Locate every Plasmodium malariae-infected red blood cell.
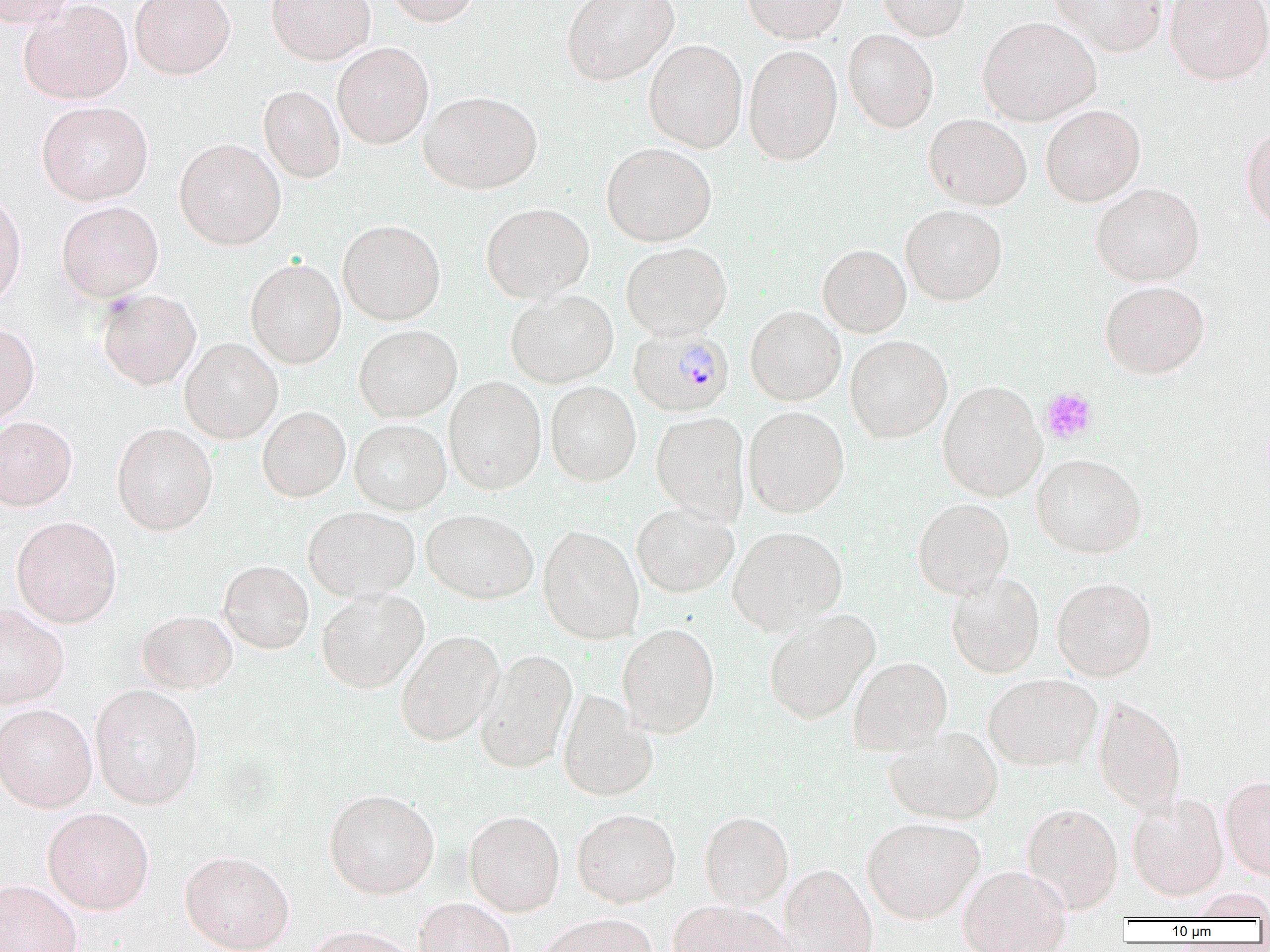
Approximate bounding boxes as (x1,y1)-(x2,y2) corner pairs in pixels.
Plasmodium malariae-infected red blood cells: (629,326)-(735,416).

{
  "slide_level_diagnosis": "Plasmodium malariae",
  "preparation": "thin blood film",
  "modality": "light microscopy",
  "uninfected_red_blood_cell_locations": "approximate bounding boxes as (x1,y1)-(x2,y2) corner pairs in pixels: (0,0)-(77,28), (130,0)-(235,79), (266,0)-(375,65), (384,0)-(481,27), (561,0)-(679,85), (742,0)-(848,43), (878,0)-(970,41), (1050,0)-(1167,56), (1165,0)-(1270,84), (19,1)-(133,105), (978,16)-(1101,125), (843,29)-(938,133), (643,39)-(748,152), (332,42)-(434,149), (743,45)-(843,165), (259,85)-(346,183), (419,90)-(543,194), (36,101)-(152,205), (1040,105)-(1145,206), (917,113)-(1018,301), (924,113)-(1032,210), (1240,124)-(1270,231), (174,138)-(286,249), (601,142)-(717,246), (1091,183)-(1204,286), (0,191)-(27,310), (56,201)-(164,301), (481,202)-(594,302), (901,204)-(1007,306), (338,219)-(445,325), (621,241)-(732,339), (817,243)-(911,337), (245,258)-(346,368), (1100,280)-(1209,378), (96,288)-(202,390), (505,289)-(618,387), (745,305)-(845,405), (0,321)-(40,425), (353,324)-(462,422), (845,334)-(952,443), (180,337)-(282,443), (444,376)-(547,495), (545,380)-(641,486), (937,380)-(1047,501), (257,406)-(351,502), (744,406)-(849,518), (651,411)-(750,524), (0,416)-(77,511), (350,419)-(451,514), (112,422)-(218,535), (1031,453)-(1147,557), (913,498)-(1014,598), (631,503)-(739,598), (303,506)-(420,602), (421,508)-(538,604), (11,515)-(122,628), (538,525)-(644,644), (727,525)-(848,634), (218,560)-(314,654), (946,572)-(1045,678), (1052,577)-(1157,681), (316,589)-(429,692), (0,603)-(69,708), (136,609)-(237,693), (763,609)-(880,724), (617,623)-(720,737), (395,630)-(505,746), (474,649)-(578,772), (848,656)-(952,755), (984,673)-(1102,770), (90,684)-(204,809), (558,690)-(658,801), (1093,695)-(1186,816), (0,703)-(97,812), (885,725)-(1003,824), (1220,776)-(1270,880), (324,789)-(439,898), (1127,792)-(1228,901), (1022,802)-(1123,913), (42,806)-(155,915), (572,808)-(681,907), (464,810)-(565,915), (699,811)-(794,908), (862,816)-(984,924), (180,850)-(294,952), (779,863)-(878,952), (958,864)-(1072,952), (0,879)-(82,952), (1189,888)-(1270,921), (414,897)-(516,952), (667,900)-(794,952), (535,914)-(659,952), (303,925)-(420,952)",
  "platelet_locations": "approximate bounding boxes as (x1,y1)-(x2,y2) corner pairs in pixels: (1040,387)-(1098,444)",
  "image_size": "1270×952 pixels",
  "field_of_view": "one of a larger specimen",
  "magnification": "1000x"
}